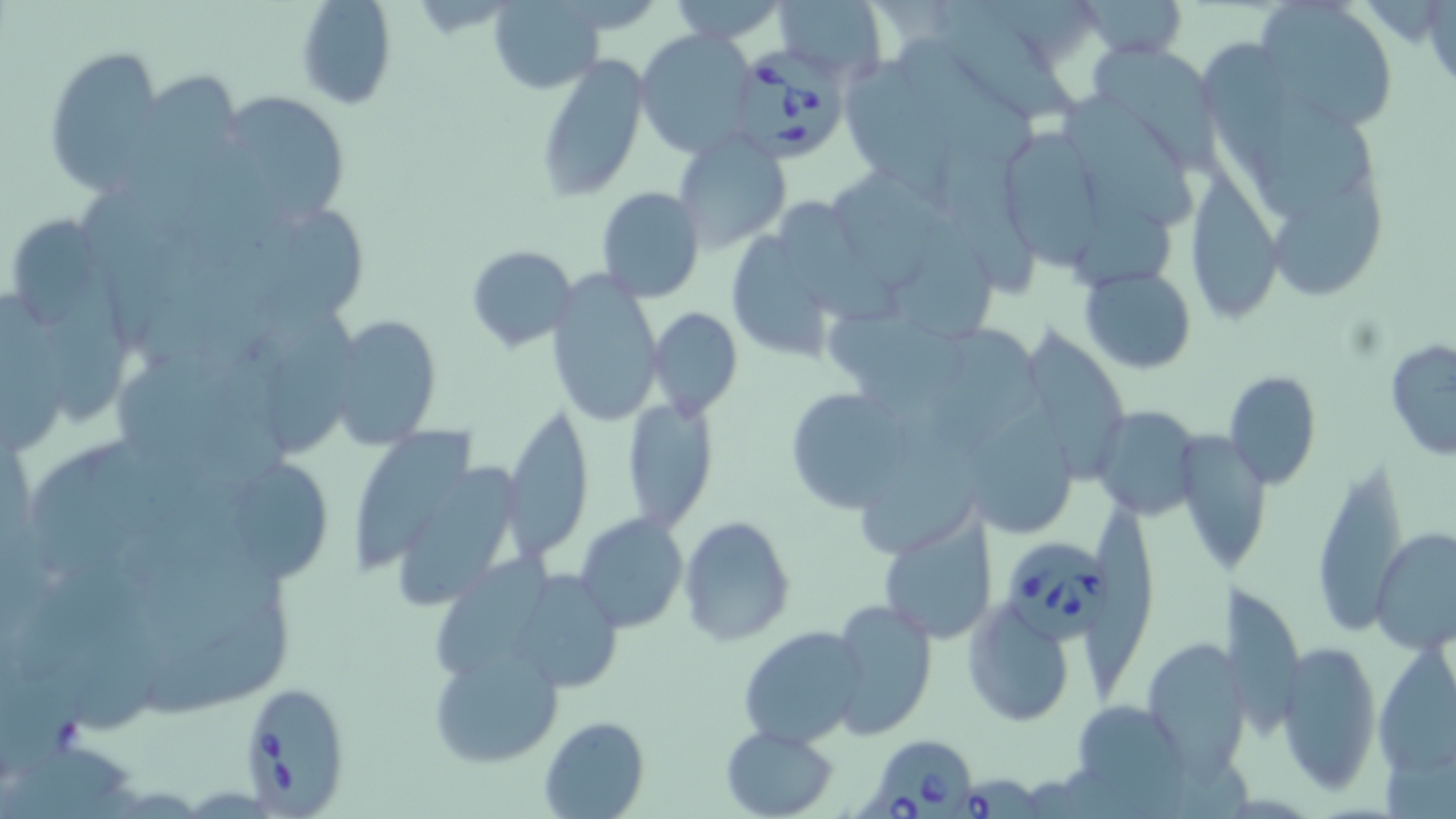

slide-level diagnosis = Babesia divergens
magnification = 1000x
Babesia divergens-infected red blood cell locations = approximate bounding boxes as (x1, y1, x2, y2) in pixels: (741, 49, 853, 164), (1006, 537, 1120, 644), (237, 683, 351, 812), (873, 742, 973, 819), (953, 772, 1051, 819)
uninfected red blood cell locations = approximate bounding boxes as (x1, y1, x2, y2) in pixels: (296, 0, 398, 111), (486, 0, 604, 94), (668, 0, 788, 44), (774, 0, 889, 78), (1082, 0, 1186, 59), (1255, 0, 1399, 132), (940, 3, 1080, 123), (636, 30, 757, 158), (902, 37, 1033, 155), (1202, 38, 1297, 181), (1087, 42, 1220, 166), (45, 48, 166, 195), (536, 57, 649, 202), (846, 64, 986, 217), (138, 69, 243, 176), (213, 91, 351, 228), (1063, 94, 1199, 220), (1254, 99, 1377, 224), (992, 123, 1109, 267), (673, 132, 791, 253), (943, 153, 1034, 294), (834, 169, 938, 291), (1181, 169, 1281, 326), (1273, 182, 1388, 300), (594, 186, 705, 301), (777, 199, 898, 321), (276, 208, 367, 330), (1078, 214, 1170, 294), (15, 219, 100, 324), (897, 221, 994, 343), (727, 228, 836, 363), (466, 245, 578, 352), (1080, 267, 1197, 373), (545, 273, 663, 427), (45, 280, 129, 418), (0, 291, 60, 456), (649, 306, 742, 420), (830, 310, 968, 410), (268, 311, 361, 458), (329, 315, 442, 449), (933, 323, 1044, 444), (1019, 323, 1132, 481), (1385, 338, 1456, 461), (1222, 370, 1324, 488), (782, 385, 916, 515), (620, 394, 722, 532), (975, 398, 1079, 534), (1091, 404, 1205, 518), (501, 405, 593, 563), (866, 418, 980, 555), (357, 424, 476, 566), (1172, 429, 1274, 579), (1311, 458, 1409, 635), (235, 464, 339, 579), (401, 465, 522, 610), (1082, 497, 1157, 700), (875, 508, 1000, 645), (575, 513, 688, 635), (679, 515, 796, 645), (1370, 527, 1455, 654), (436, 555, 552, 681), (525, 573, 621, 688), (1221, 582, 1303, 738), (828, 598, 937, 739), (960, 601, 1076, 729), (146, 606, 293, 725), (739, 626, 866, 750), (1138, 637, 1245, 772), (1276, 639, 1381, 793), (430, 645, 564, 770), (1374, 651, 1454, 777), (1065, 699, 1196, 809), (539, 714, 650, 818), (721, 724, 838, 818)
modality = light microscopy
preparation = thin blood film
stain = May-Grünwald-Giemsa
image size = 1456×819 pixels
field of view = single